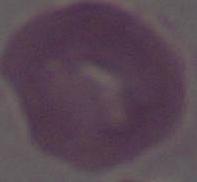

Captured at 1000x magnification. Micrograph. An erythrocyte is shown.